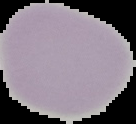
Summary:
  - Preparation: thin blood smear
  - Image type: segmented cell region on a black background
  - Malaria status: uninfected
  - Image size: 136×124 pixels